Classify this cell by malaria status.
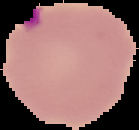
Parasitized.

Image is 139×130 pixels. The area outside the segmented cell region is set to black. From a thin blood film.